Comment on the morphology of the red blood cells.
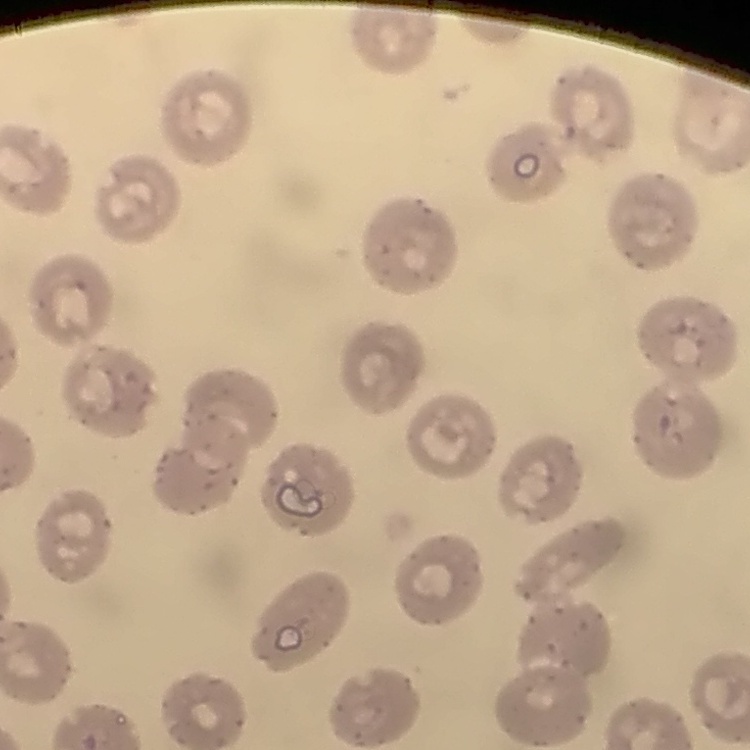
No rouleaux formation.

Thin peripheral smear. Stained with either Field's or Giemsa. Square crop of a larger photomicrograph.